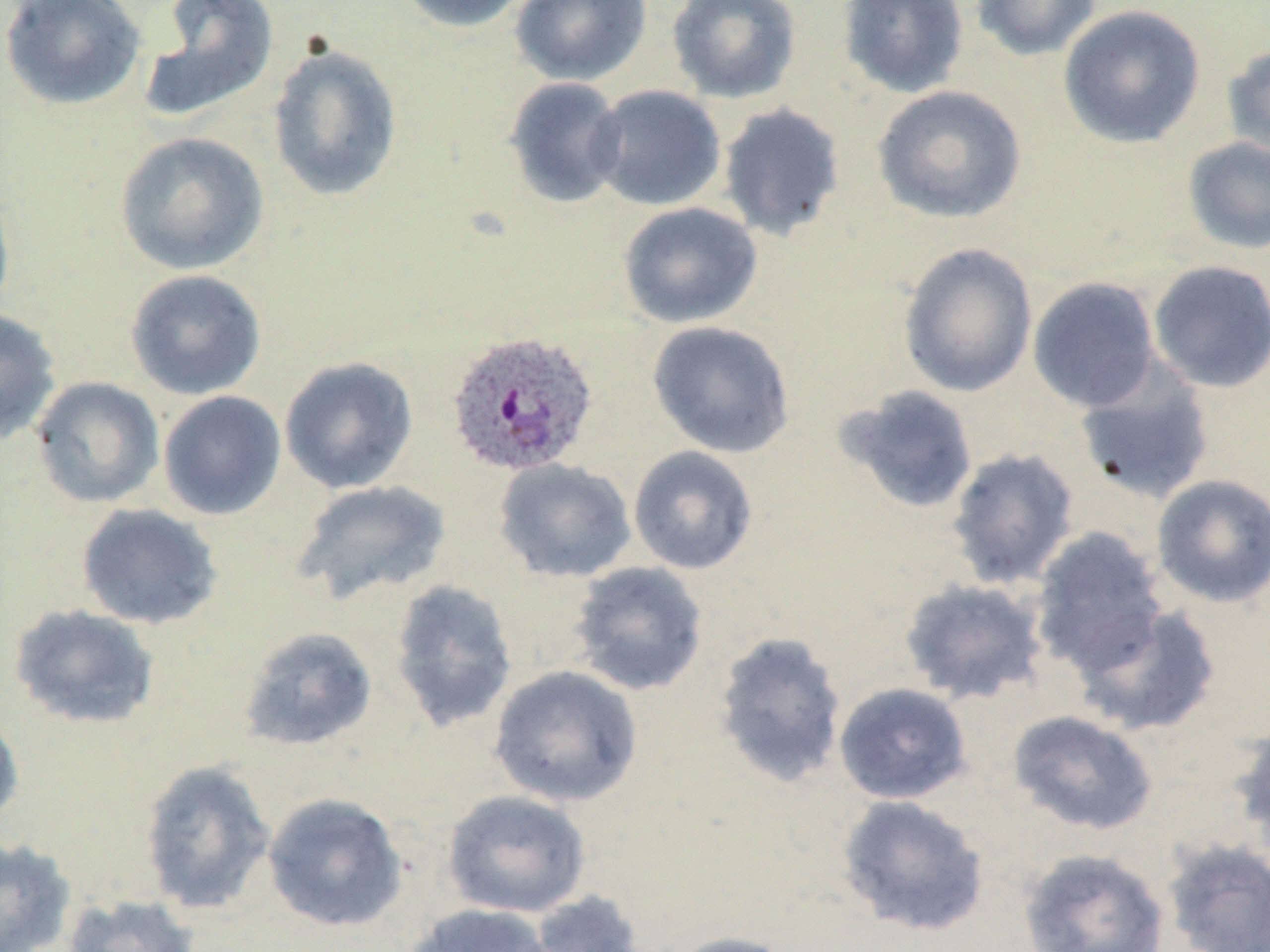
Approximate bounding boxes as named x1/y1/x2/y2 corners in pixels. Uninfected red blood cell locations: (x1=0, y1=0, x2=146, y2=112), (x1=137, y1=0, x2=279, y2=124), (x1=393, y1=0, x2=534, y2=34), (x1=510, y1=0, x2=652, y2=86), (x1=666, y1=0, x2=802, y2=104), (x1=838, y1=0, x2=969, y2=99), (x1=970, y1=0, x2=1103, y2=62), (x1=1058, y1=5, x2=1206, y2=148), (x1=267, y1=41, x2=403, y2=202), (x1=1222, y1=42, x2=1270, y2=163), (x1=504, y1=76, x2=628, y2=209), (x1=588, y1=85, x2=726, y2=211), (x1=872, y1=85, x2=1028, y2=224), (x1=717, y1=103, x2=846, y2=242), (x1=114, y1=131, x2=270, y2=275), (x1=1182, y1=136, x2=1270, y2=254), (x1=0, y1=180, x2=16, y2=322), (x1=617, y1=201, x2=762, y2=328), (x1=898, y1=243, x2=1038, y2=397), (x1=1147, y1=260, x2=1270, y2=393), (x1=125, y1=269, x2=267, y2=400), (x1=1027, y1=276, x2=1161, y2=412), (x1=0, y1=307, x2=61, y2=446), (x1=647, y1=321, x2=795, y2=458), (x1=279, y1=356, x2=419, y2=495), (x1=1074, y1=359, x2=1216, y2=505), (x1=29, y1=376, x2=165, y2=508), (x1=835, y1=384, x2=979, y2=514), (x1=158, y1=390, x2=286, y2=521), (x1=628, y1=445, x2=758, y2=575), (x1=945, y1=447, x2=1081, y2=590), (x1=493, y1=458, x2=637, y2=583), (x1=1150, y1=474, x2=1270, y2=608), (x1=291, y1=479, x2=452, y2=605), (x1=76, y1=503, x2=223, y2=629), (x1=1029, y1=526, x2=1170, y2=675), (x1=568, y1=560, x2=709, y2=696), (x1=898, y1=578, x2=1050, y2=705), (x1=389, y1=579, x2=518, y2=732), (x1=1070, y1=602, x2=1222, y2=736), (x1=9, y1=604, x2=160, y2=730), (x1=239, y1=626, x2=378, y2=752), (x1=713, y1=631, x2=848, y2=787), (x1=488, y1=664, x2=643, y2=807), (x1=833, y1=682, x2=972, y2=804), (x1=0, y1=708, x2=24, y2=832), (x1=1007, y1=710, x2=1159, y2=836), (x1=1229, y1=719, x2=1270, y2=862), (x1=139, y1=760, x2=277, y2=916), (x1=441, y1=790, x2=592, y2=918), (x1=262, y1=792, x2=409, y2=932), (x1=836, y1=794, x2=990, y2=937), (x1=0, y1=837, x2=77, y2=952), (x1=1161, y1=838, x2=1270, y2=952), (x1=1017, y1=848, x2=1171, y2=952), (x1=526, y1=890, x2=646, y2=952), (x1=60, y1=893, x2=202, y2=952), (x1=402, y1=903, x2=556, y2=952), (x1=664, y1=931, x2=798, y2=952). Plasmodium ovale-infected red blood cell locations: (x1=443, y1=330, x2=600, y2=479). Slide-level diagnosis: Plasmodium ovale. Light microscopy. Captured at 1000x magnification. Image is 1270×952 pixels. Thin blood smear. May-Grünwald-Giemsa-stained preparation. One field of a larger specimen.